Comment on the morphology of the erythrocytes.
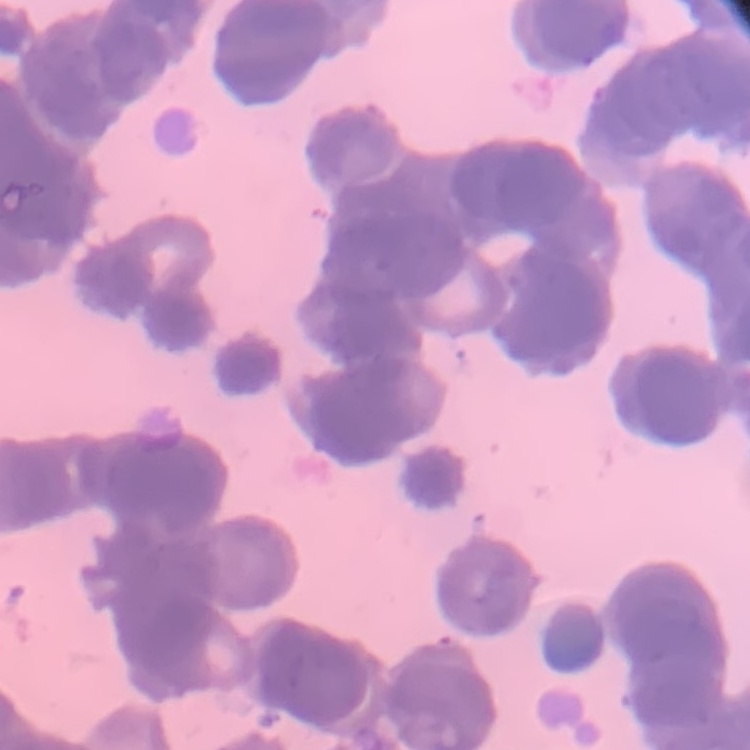
Rouleaux formation.

One tile cut from a larger photomicrograph. Thin peripheral smear. Field's or Giemsa stain.